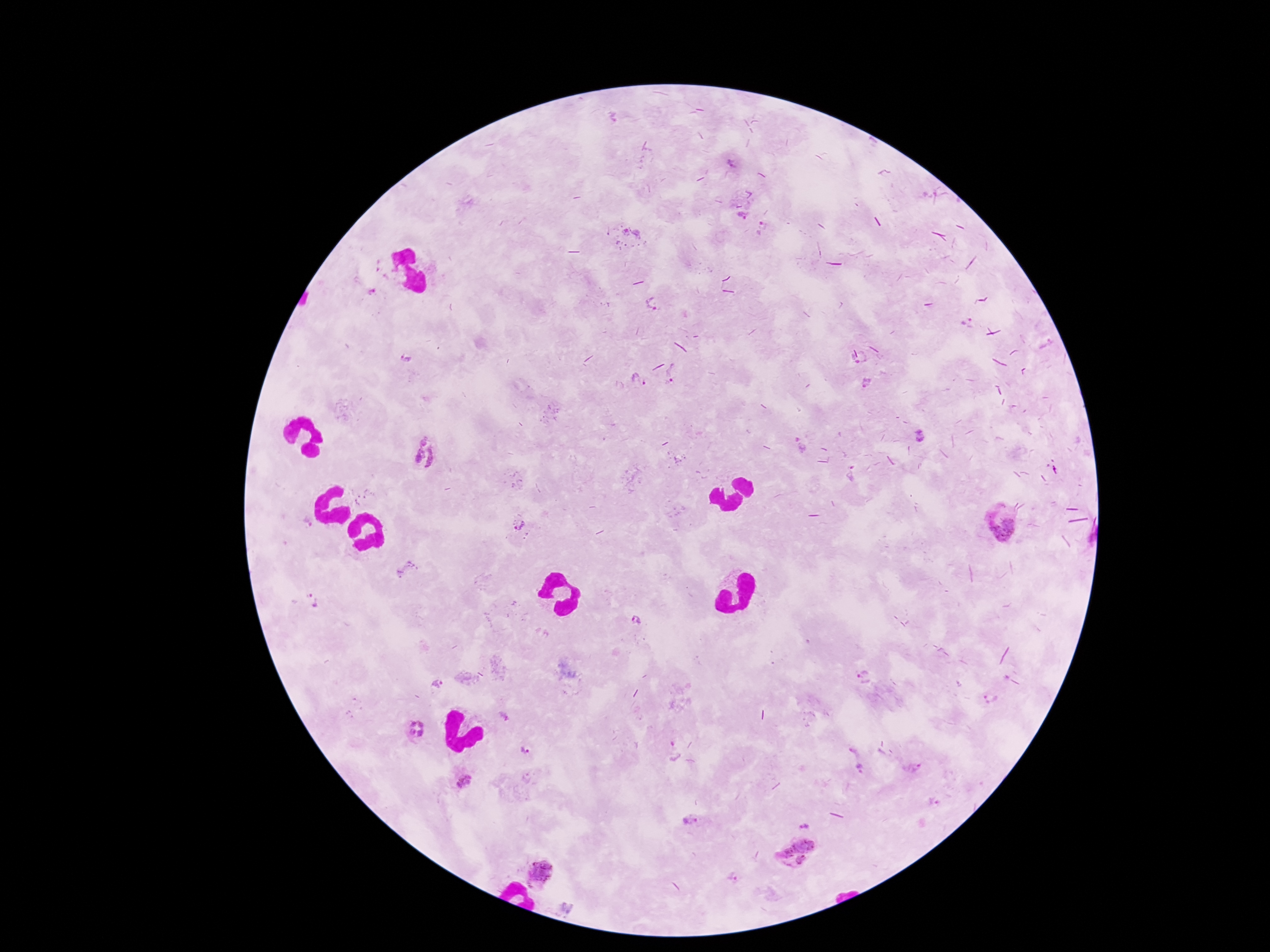
magnification: 100x
plasmodium_parasite_locations: 'approximate centers as {x, y} in pixels: {733, 164}, {743, 217}, {630, 235}, {660, 303}, {970, 322}, {406, 358}, {860, 360}, {675, 375}, {639, 381}, {867, 382}, {921, 435}, {798, 444}, {424, 453}, {365, 499}, {521, 523}, {1004, 528}, {408, 570}, {314, 600}, {637, 621}, {862, 677}, {438, 684}, {417, 730}, {524, 750}, {673, 750}, {914, 769}, {464, 781}, {933, 802}, {690, 820}, {804, 826}, {794, 848}, {801, 861}, {541, 874}, {733, 877}'
capture: smartphone camera through the microscope eyepiece
image_size: 1270×952 pixels
field_of_view: one from this slide
preparation: thick blood film
patient_malaria_status: infected
stain: Giemsa